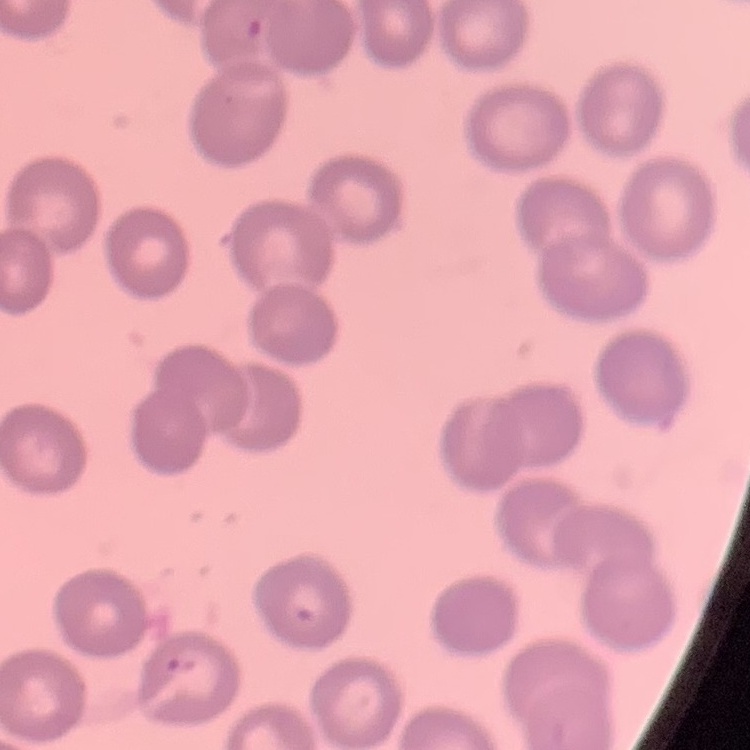 The red blood cells exhibit no rouleaux formation. Stained with either Field's or Giemsa. Thin peripheral smear. One tile cut from a larger photomicrograph.